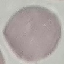

Result: no malaria parasites seen. Giemsa stain. Automatically extracted cell patch, resized to 64 × 64 pixels. Thin smear of blood. Acquired by smartphone through the microscope eyepiece.